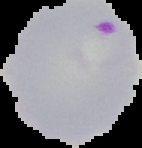
malaria status = parasitized
image size = 142×148 pixels
image type = segmented cell region with the area outside set to black
preparation = thin blood film